Identify the parasite.
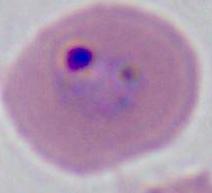

This is Plasmodium.

magnification = 400x or 1000x
modality = micrograph